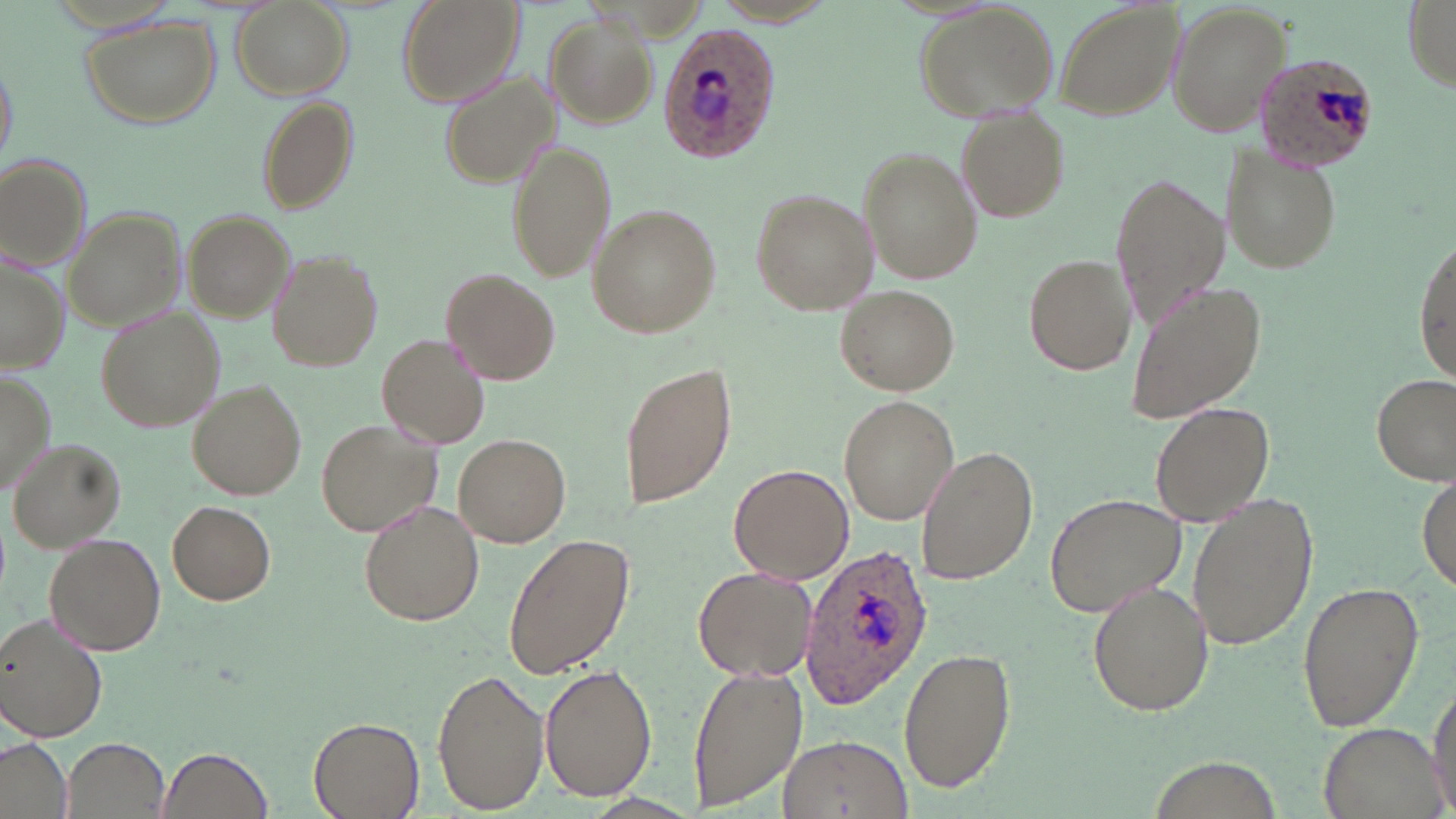

Summary:
  - Coordinate format: approximate bounding boxes as (x1,y1)-(x2,y2) corner pairs in pixels
  - Uninfected red blood cell locations: (396,0)-(523,109), (1054,0)-(1184,120), (1166,0)-(1291,139), (1402,0)-(1454,88), (230,1)-(352,101), (912,4)-(1062,121), (543,13)-(656,123), (80,14)-(222,129), (0,51)-(17,172), (441,70)-(561,189), (255,96)-(360,218), (955,109)-(1069,224), (505,136)-(617,284), (1218,145)-(1343,276), (861,147)-(982,287), (1,155)-(92,267), (1109,169)-(1228,332), (747,188)-(878,317), (590,205)-(720,336), (64,207)-(185,334), (185,209)-(295,324), (1414,243)-(1455,378), (268,250)-(383,372), (1023,251)-(1136,377), (0,255)-(69,374), (442,268)-(557,384), (1123,277)-(1267,426), (838,285)-(957,396), (96,307)-(223,431), (376,333)-(490,450), (617,357)-(737,515), (0,368)-(53,496), (1371,372)-(1455,486), (190,382)-(307,498), (839,395)-(958,526), (1150,400)-(1276,527), (316,417)-(440,536), (453,434)-(571,547), (8,438)-(126,550), (917,446)-(1038,584), (728,463)-(854,584), (1417,474)-(1454,592), (1046,492)-(1187,616), (1185,496)-(1318,653), (167,500)-(275,605), (360,501)-(483,627), (504,531)-(637,681), (44,534)-(166,655), (692,564)-(817,682), (1088,581)-(1213,718), (1296,581)-(1424,734), (0,613)-(105,740), (899,644)-(1016,795), (687,663)-(808,812), (539,665)-(656,801), (433,669)-(549,813), (1427,678)-(1456,817), (308,716)-(424,819), (1316,723)-(1444,819), (777,733)-(911,819), (63,736)-(168,817), (1,739)-(69,819), (158,746)-(276,819)
  - Plasmodium ovale-infected red blood cell locations: (657,23)-(780,164), (1250,53)-(1379,172), (800,542)-(932,706)
  - Slide-level diagnosis: Plasmodium ovale
  - Stain: May-Grünwald-Giemsa
  - Image size: 1456×819 pixels
  - Magnification: 1000x
  - Modality: optical microscopy
  - Field of view: single
  - Preparation: thin blood film